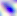
modality = photomicrograph
identification = Toxoplasma gondii
magnification = 400x